Give the extent of all Plasmodium ovale-infected red blood cells.
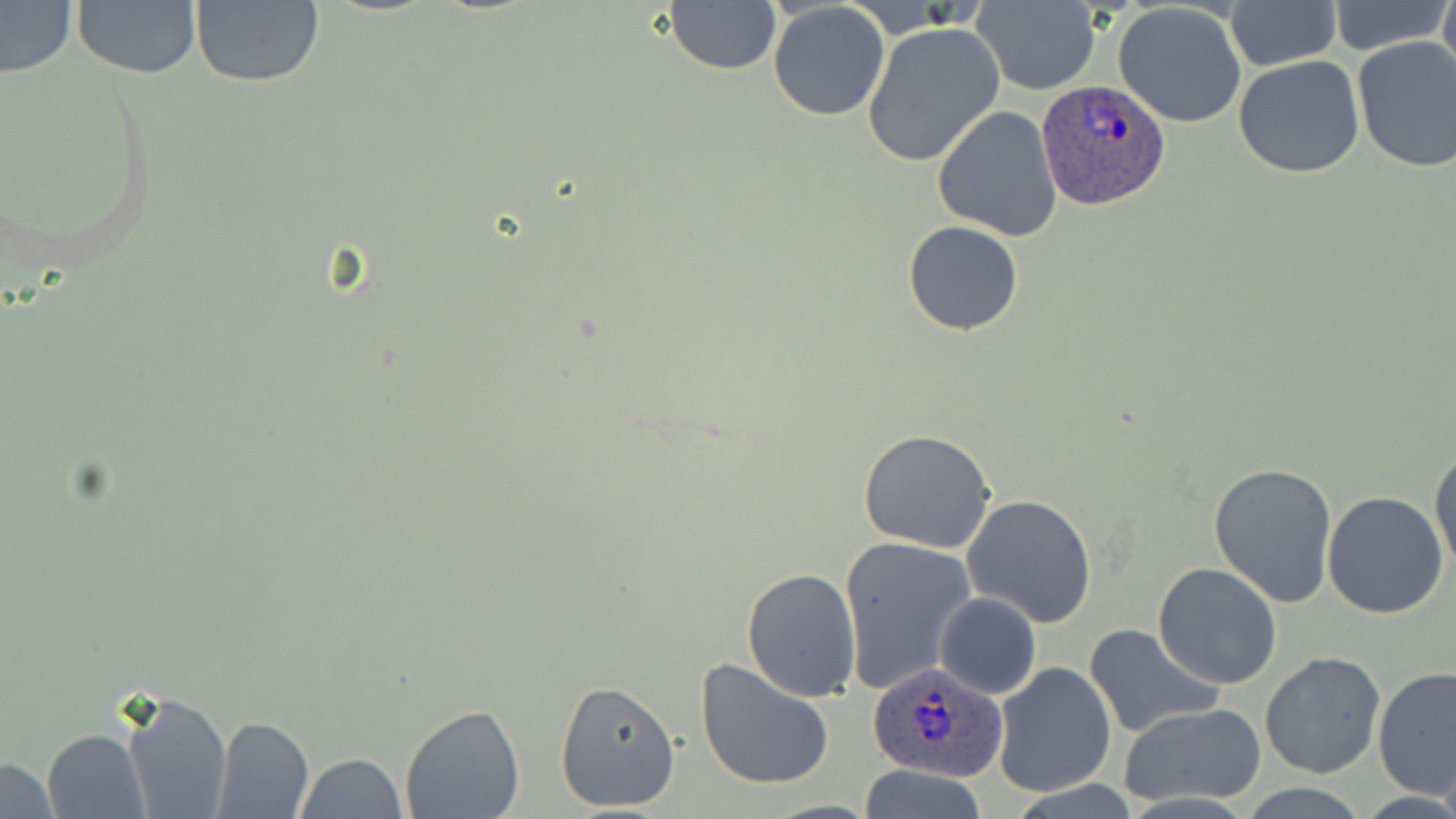

Approximate bounding boxes as named x1/y1/x2/y2 corners in pixels.
Plasmodium ovale-infected red blood cells: (x1=1037, y1=79, x2=1170, y2=211), (x1=865, y1=661, x2=1007, y2=782).

slide_level_diagnosis: Plasmodium ovale
preparation: thin blood smear
uninfected_red_blood_cell_locations: 'approximate bounding boxes as named x1/y1/x2/y2 corners in pixels: (x1=191, y1=0, x2=325, y2=89), (x1=1438, y1=0, x2=1456, y2=85), (x1=663, y1=1, x2=781, y2=77), (x1=767, y1=1, x2=891, y2=121), (x1=970, y1=1, x2=1101, y2=94), (x1=1227, y1=1, x2=1339, y2=71), (x1=74, y1=2, x2=201, y2=79), (x1=1328, y1=2, x2=1450, y2=56), (x1=0, y1=3, x2=76, y2=79), (x1=1113, y1=3, x2=1248, y2=128), (x1=862, y1=22, x2=1004, y2=166), (x1=1351, y1=38, x2=1456, y2=174), (x1=1233, y1=55, x2=1366, y2=179), (x1=932, y1=105, x2=1063, y2=241), (x1=902, y1=220, x2=1025, y2=336), (x1=857, y1=429, x2=997, y2=554), (x1=1428, y1=444, x2=1456, y2=577), (x1=1208, y1=461, x2=1339, y2=608), (x1=1322, y1=491, x2=1448, y2=620), (x1=962, y1=493, x2=1098, y2=628), (x1=839, y1=535, x2=976, y2=697), (x1=1153, y1=562, x2=1283, y2=689), (x1=740, y1=567, x2=861, y2=703), (x1=934, y1=592, x2=1040, y2=698), (x1=1086, y1=624, x2=1222, y2=740), (x1=1260, y1=651, x2=1386, y2=778), (x1=693, y1=656, x2=838, y2=792), (x1=992, y1=661, x2=1116, y2=798), (x1=1374, y1=668, x2=1455, y2=798), (x1=554, y1=677, x2=681, y2=813), (x1=120, y1=687, x2=230, y2=819), (x1=1118, y1=702, x2=1267, y2=807), (x1=399, y1=704, x2=526, y2=819), (x1=212, y1=716, x2=313, y2=817), (x1=41, y1=729, x2=147, y2=817), (x1=293, y1=754, x2=407, y2=819), (x1=0, y1=759, x2=60, y2=816), (x1=856, y1=764, x2=988, y2=819)'
field_of_view: single
stain: May-Grünwald-Giemsa
image_size: 1456×819 pixels
modality: optical microscopy
magnification: 1000x